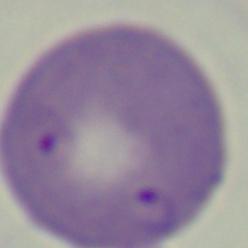
Summary:
  - Identification: Babesia
  - Magnification: 1000x
  - Modality: photomicrograph